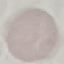
Malaria status: uninfected. Cell patch, automatically extracted from a larger field of view and resized to 64 × 64 pixels. Giemsa-stained preparation. Thin blood film. Acquired by smartphone through the microscope eyepiece.